Report the malaria status of this cell.
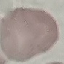

It is uninfected.

Automatically extracted cell patch, resized to 64 × 64 pixels. Giemsa stain. Photographed with a smartphone camera at the microscope eyepiece. Thin smear of blood.